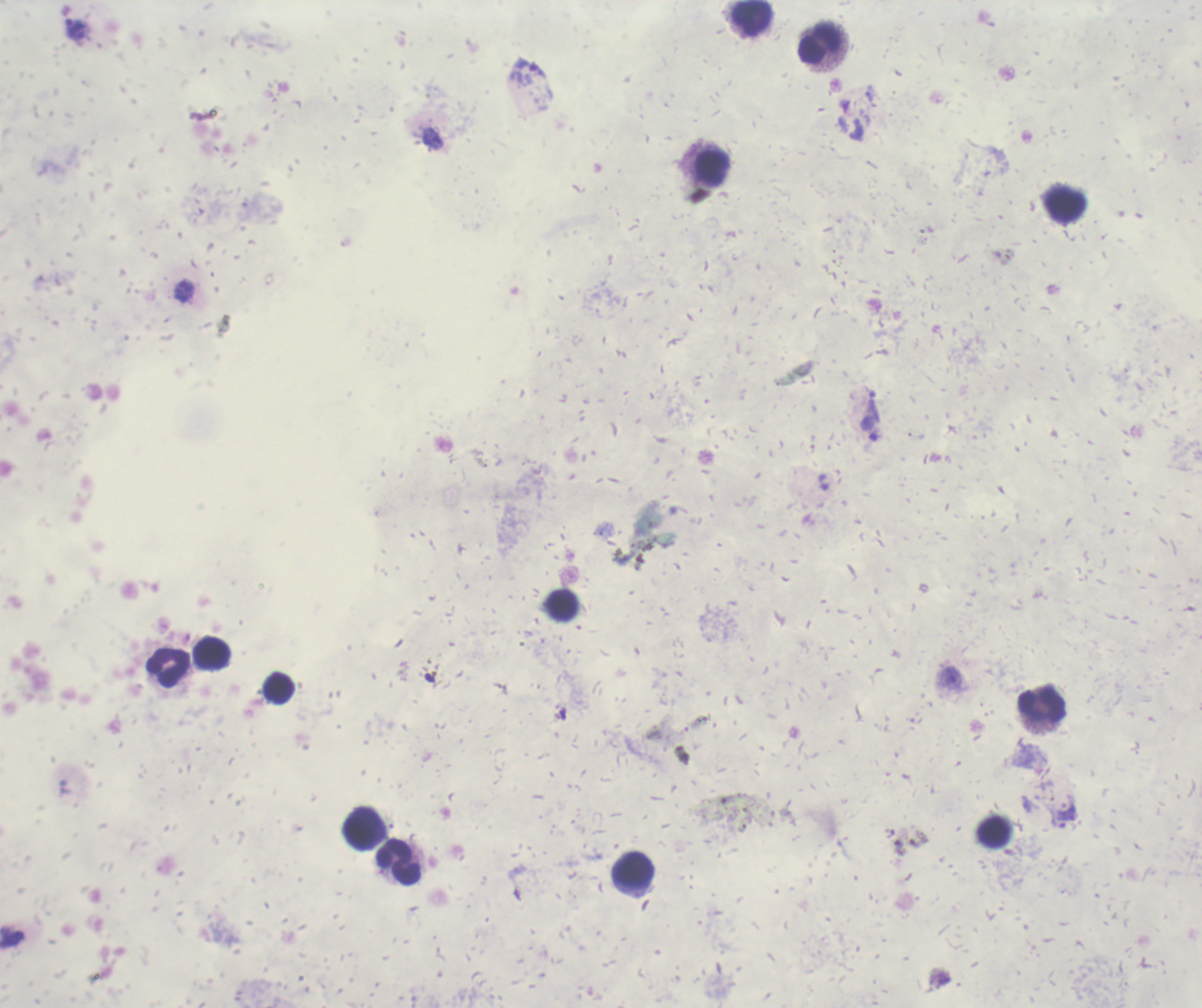
coordinate format = approximate centers as (x, y) in pixels
trophozoite locations = (869, 430), (951, 678), (1066, 813)
leukocyte locations = (751, 18), (820, 44), (712, 168), (1065, 205), (562, 606), (212, 653), (168, 668), (279, 688), (1042, 706), (364, 827), (994, 832), (398, 862), (635, 872)
result = Plasmodium parasites detected
coloration quality = bad
field of view = one from this slide
background quality = unsatisfactory
magnification = 100x
preparation = thick blood smear
image size = 1202×1008 pixels
stain = Romanowsky
context = previously used in an actual diagnosis